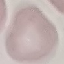 Result: no malaria parasites seen. Cell patch, automatically extracted from a larger field of view and resized to 64 × 64 pixels. Giemsa-stained preparation. Thin blood smear. Photographed with a smartphone camera at the microscope eyepiece.